State which cell type is depicted.
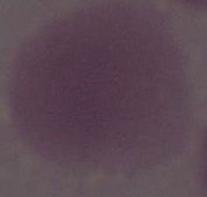

An erythrocyte.

Summary:
  - Magnification: 1000x
  - Modality: photomicrograph